Outline each Plasmodium ovale-infected red blood cell.
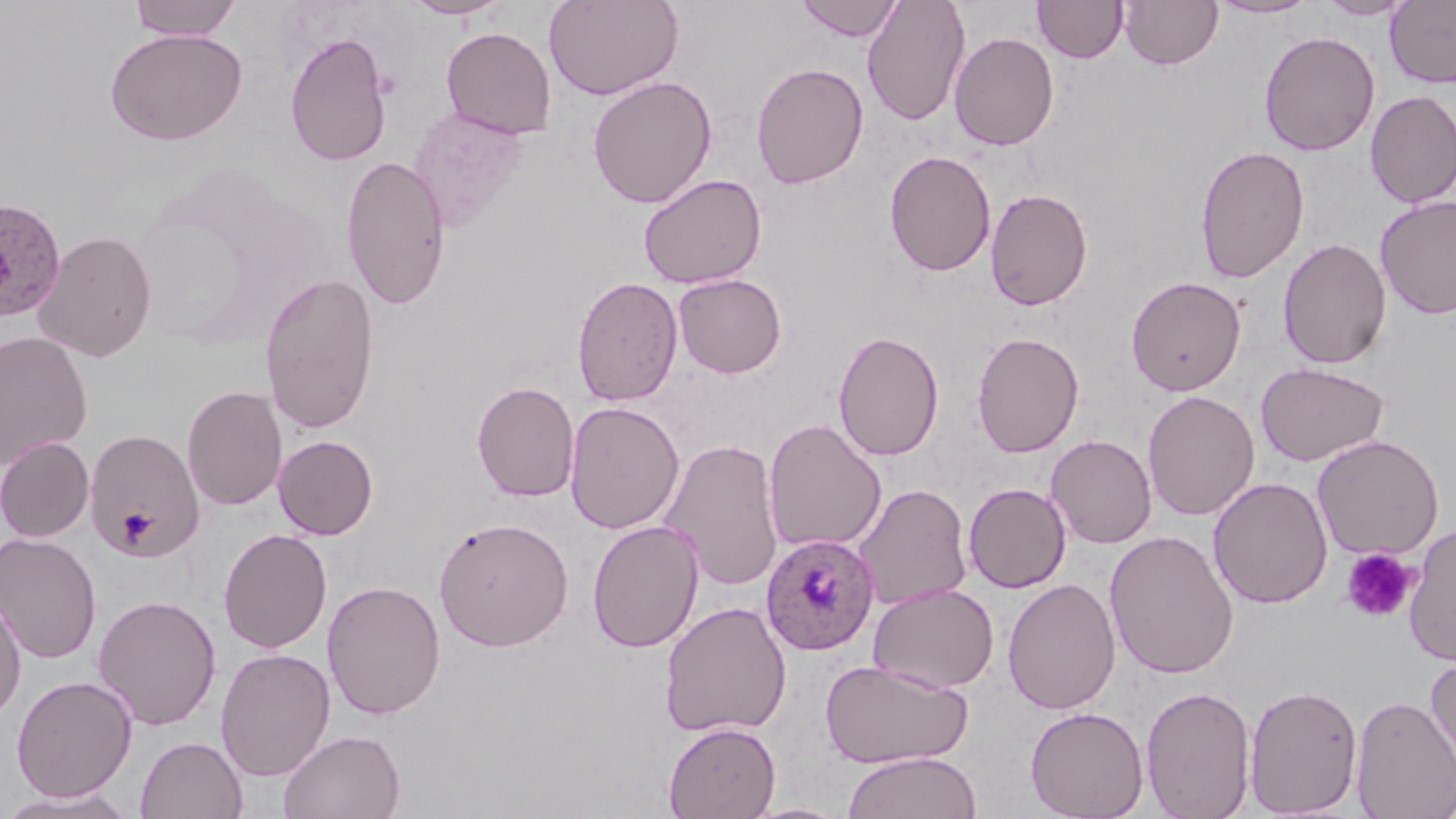
Approximate bounding boxes as (x1,y1)-(x2,y2) corner pairs in pixels.
Plasmodium ovale-infected red blood cells: (0,197)-(67,322), (761,533)-(879,655).

{
  "slide_level_diagnosis": "Plasmodium ovale",
  "image_size": "1456×819 pixels",
  "uninfected_red_blood_cell_locations": "approximate bounding boxes as (x1,y1)-(x2,y2) corner pairs in pixels: (127,0)-(243,41), (403,0)-(511,20), (544,0)-(683,100), (794,0)-(906,42), (861,0)-(971,126), (1032,0)-(1128,63), (1119,0)-(1224,70), (1208,0)-(1319,18), (1317,0)-(1417,20), (1386,0)-(1456,88), (441,26)-(556,139), (104,27)-(247,145), (284,30)-(393,167), (1259,31)-(1380,156), (949,32)-(1059,151), (751,62)-(869,190), (587,75)-(717,209), (1365,90)-(1456,208), (407,107)-(528,231), (1195,144)-(1310,284), (884,150)-(996,277), (340,154)-(451,312), (638,173)-(767,289), (985,188)-(1093,311), (1375,195)-(1456,320), (33,229)-(158,362), (1277,237)-(1391,369), (260,271)-(380,434), (673,273)-(787,378), (1126,275)-(1246,395), (572,276)-(683,406), (833,329)-(944,461), (0,331)-(94,468), (971,331)-(1085,457), (1255,361)-(1390,467), (472,380)-(580,502), (181,385)-(287,511), (1142,390)-(1260,521), (564,401)-(684,534), (763,418)-(886,553), (85,428)-(204,562), (1046,434)-(1157,548), (273,435)-(378,540), (1312,435)-(1445,560), (0,437)-(94,542), (660,439)-(784,591), (1208,477)-(1333,608), (963,483)-(1071,593), (854,484)-(972,610), (434,516)-(574,651), (586,519)-(704,654), (1403,523)-(1456,666), (218,528)-(332,653), (1103,529)-(1240,680), (0,533)-(102,663), (1002,578)-(1121,715), (322,580)-(446,720), (868,582)-(999,693), (0,593)-(27,723), (93,595)-(221,730), (659,601)-(792,737), (214,647)-(336,781), (1425,655)-(1456,779), (819,658)-(973,768), (12,674)-(137,802), (1244,682)-(1364,816), (1140,684)-(1257,818), (1350,694)-(1456,819), (1025,705)-(1150,819), (663,721)-(780,818), (278,728)-(406,819), (135,735)-(248,819), (842,751)-(982,819), (0,788)-(141,819), (739,801)-(853,819)",
  "field_of_view": "single",
  "platelet_locations": "approximate bounding boxes as (x1,y1)-(x2,y2) corner pairs in pixels: (115,508)-(157,547), (1341,548)-(1418,623)",
  "magnification": "1000x",
  "modality": "light microscopy",
  "stain": "May-Grünwald-Giemsa",
  "preparation": "thin blood film"
}